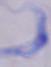
identification = trypanosome
modality = photomicrograph
magnification = 1000x